Describe the morphology of the red blood cells.
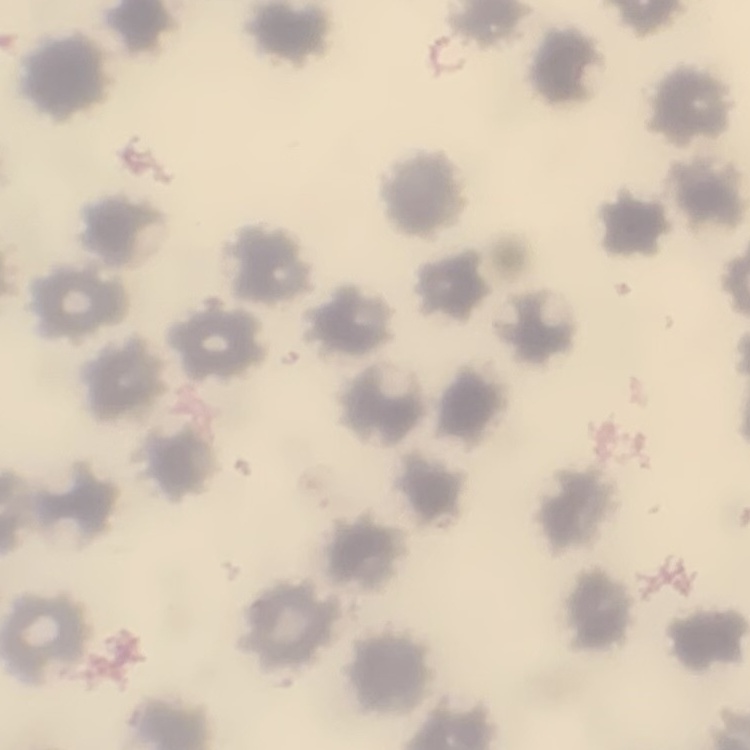
No rouleaux formation.

Field's or Giemsa stain. Thin blood smear. One tile cut from a larger photomicrograph.